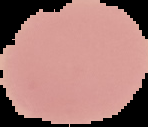
Summary:
  - Malaria status: uninfected
  - Preparation: thin blood film
  - Image size: 148×127 pixels
  - Image type: segmented cell region with the area outside set to black